Classify this cell by malaria status.
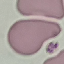

It is uninfected.

image type = automatically extracted cell patch, resized to 64 × 64 pixels
preparation = thin smear
capture = smartphone camera at the microscope eyepiece
stain = Giemsa